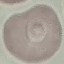

Result: no malaria parasites seen. Thin blood film. Cell patch, automatically extracted from a larger field of view and resized to 64 × 64 pixels. Giemsa-stained preparation. Acquired by smartphone through the microscope eyepiece.